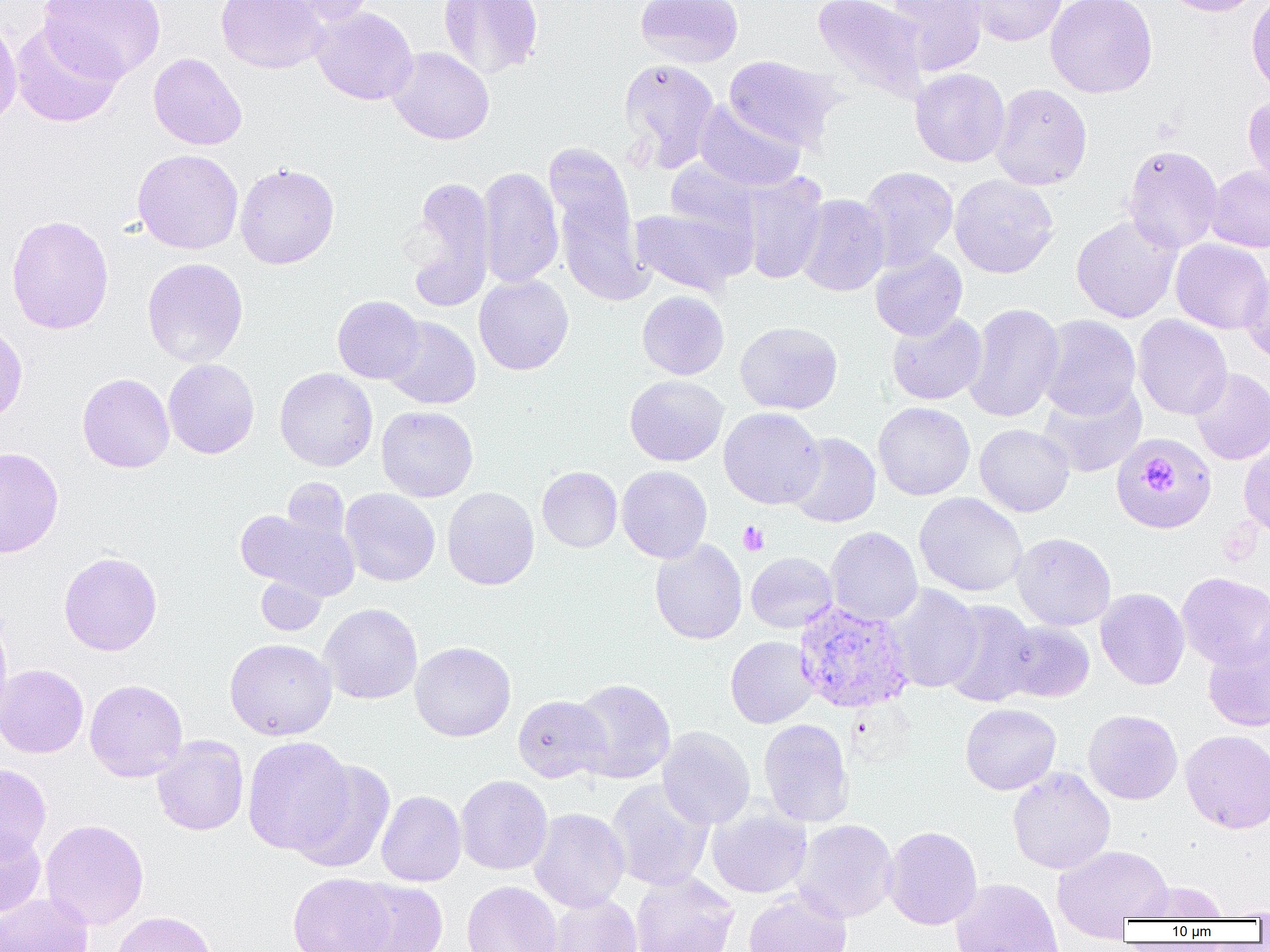
{
  "slide_level_diagnosis": "Plasmodium vivax",
  "modality": "optical microscopy",
  "preparation": "thin blood film",
  "magnification": "1000x",
  "image_size": "1270×952 pixels",
  "plasmodium_vivax_infected_red_blood_cell_locations": "approximate bounding boxes as named x1/y1/x2/y2 corners in pixels: (x1=793, y1=601, x2=914, y2=714)",
  "uninfected_red_blood_cell_locations": "approximate bounding boxes as named x1/y1/x2/y2 corners in pixels: (x1=39, y1=0, x2=165, y2=83), (x1=215, y1=0, x2=329, y2=74), (x1=269, y1=0, x2=377, y2=25), (x1=438, y1=0, x2=544, y2=80), (x1=636, y1=0, x2=743, y2=67), (x1=812, y1=0, x2=929, y2=104), (x1=885, y1=0, x2=988, y2=75), (x1=965, y1=0, x2=1068, y2=46), (x1=1045, y1=0, x2=1157, y2=98), (x1=1161, y1=0, x2=1264, y2=16), (x1=1247, y1=0, x2=1270, y2=100), (x1=310, y1=7, x2=418, y2=105), (x1=0, y1=13, x2=22, y2=129), (x1=10, y1=22, x2=124, y2=128), (x1=386, y1=46, x2=495, y2=145), (x1=148, y1=53, x2=247, y2=150), (x1=724, y1=55, x2=843, y2=151), (x1=619, y1=59, x2=720, y2=171), (x1=910, y1=68, x2=1010, y2=167), (x1=990, y1=83, x2=1092, y2=190), (x1=1243, y1=96, x2=1270, y2=192), (x1=693, y1=100, x2=806, y2=192), (x1=546, y1=142, x2=648, y2=305), (x1=1123, y1=144, x2=1223, y2=253), (x1=132, y1=149, x2=244, y2=254), (x1=664, y1=159, x2=762, y2=246), (x1=235, y1=162, x2=340, y2=269), (x1=859, y1=166, x2=958, y2=270), (x1=1206, y1=166, x2=1270, y2=252), (x1=477, y1=167, x2=564, y2=289), (x1=738, y1=173, x2=828, y2=284), (x1=949, y1=174, x2=1058, y2=278), (x1=402, y1=177, x2=497, y2=313), (x1=797, y1=194, x2=889, y2=296), (x1=630, y1=206, x2=749, y2=296), (x1=6, y1=214, x2=114, y2=335), (x1=1071, y1=214, x2=1182, y2=324), (x1=1170, y1=239, x2=1270, y2=334), (x1=870, y1=248, x2=967, y2=341), (x1=141, y1=257, x2=249, y2=368), (x1=1239, y1=266, x2=1270, y2=366), (x1=473, y1=274, x2=574, y2=375), (x1=637, y1=290, x2=729, y2=379), (x1=332, y1=295, x2=425, y2=384), (x1=964, y1=303, x2=1065, y2=423), (x1=887, y1=311, x2=987, y2=405), (x1=1037, y1=314, x2=1141, y2=419), (x1=1133, y1=314, x2=1232, y2=420), (x1=382, y1=316, x2=480, y2=409), (x1=735, y1=321, x2=843, y2=414), (x1=0, y1=322, x2=28, y2=424), (x1=163, y1=358, x2=259, y2=459), (x1=274, y1=368, x2=377, y2=472), (x1=1189, y1=368, x2=1270, y2=465), (x1=77, y1=373, x2=174, y2=473), (x1=625, y1=375, x2=728, y2=466), (x1=1037, y1=383, x2=1147, y2=478), (x1=873, y1=401, x2=975, y2=500), (x1=377, y1=406, x2=478, y2=501), (x1=719, y1=407, x2=825, y2=509), (x1=975, y1=424, x2=1075, y2=516), (x1=786, y1=432, x2=881, y2=528), (x1=1111, y1=432, x2=1215, y2=534), (x1=1239, y1=436, x2=1270, y2=540), (x1=0, y1=446, x2=64, y2=558), (x1=616, y1=465, x2=712, y2=563), (x1=537, y1=466, x2=622, y2=552), (x1=442, y1=487, x2=540, y2=590), (x1=340, y1=488, x2=440, y2=586), (x1=913, y1=492, x2=1028, y2=597), (x1=236, y1=505, x2=360, y2=602), (x1=825, y1=526, x2=923, y2=626), (x1=1011, y1=532, x2=1116, y2=630), (x1=650, y1=539, x2=747, y2=644), (x1=59, y1=552, x2=162, y2=656), (x1=746, y1=552, x2=838, y2=633), (x1=1176, y1=572, x2=1270, y2=670), (x1=256, y1=576, x2=327, y2=636), (x1=884, y1=584, x2=983, y2=693), (x1=1095, y1=588, x2=1190, y2=690), (x1=940, y1=600, x2=1040, y2=707), (x1=319, y1=603, x2=423, y2=704), (x1=0, y1=610, x2=12, y2=729), (x1=1000, y1=621, x2=1095, y2=703), (x1=1203, y1=635, x2=1270, y2=733), (x1=725, y1=636, x2=818, y2=728), (x1=225, y1=638, x2=337, y2=740), (x1=410, y1=641, x2=516, y2=741), (x1=0, y1=664, x2=88, y2=758), (x1=568, y1=678, x2=676, y2=784), (x1=85, y1=679, x2=187, y2=782), (x1=513, y1=694, x2=610, y2=783), (x1=960, y1=703, x2=1061, y2=794), (x1=1083, y1=709, x2=1183, y2=804), (x1=758, y1=718, x2=855, y2=828), (x1=657, y1=726, x2=755, y2=829), (x1=1180, y1=729, x2=1270, y2=833), (x1=151, y1=735, x2=249, y2=835), (x1=242, y1=736, x2=356, y2=857), (x1=291, y1=760, x2=395, y2=873), (x1=0, y1=763, x2=52, y2=861), (x1=1007, y1=767, x2=1115, y2=875), (x1=455, y1=775, x2=553, y2=875), (x1=606, y1=779, x2=714, y2=891), (x1=376, y1=790, x2=466, y2=886), (x1=706, y1=805, x2=812, y2=898), (x1=529, y1=808, x2=630, y2=913), (x1=40, y1=819, x2=149, y2=930), (x1=791, y1=820, x2=898, y2=923), (x1=883, y1=826, x2=982, y2=930), (x1=0, y1=828, x2=46, y2=919), (x1=1053, y1=845, x2=1172, y2=936), (x1=631, y1=871, x2=738, y2=952), (x1=288, y1=872, x2=397, y2=952), (x1=950, y1=878, x2=1064, y2=952), (x1=346, y1=879, x2=448, y2=952), (x1=462, y1=881, x2=562, y2=952), (x1=1132, y1=881, x2=1227, y2=921), (x1=744, y1=889, x2=852, y2=952), (x1=0, y1=893, x2=93, y2=952), (x1=546, y1=894, x2=641, y2=952), (x1=1216, y1=905, x2=1270, y2=920), (x1=111, y1=911, x2=217, y2=952)",
  "platelet_locations": "approximate bounding boxes as named x1/y1/x2/y2 corners in pixels: (x1=1142, y1=457, x2=1183, y2=498), (x1=738, y1=521, x2=769, y2=556)",
  "field_of_view": "single"
}